Identify the blood parasite species.
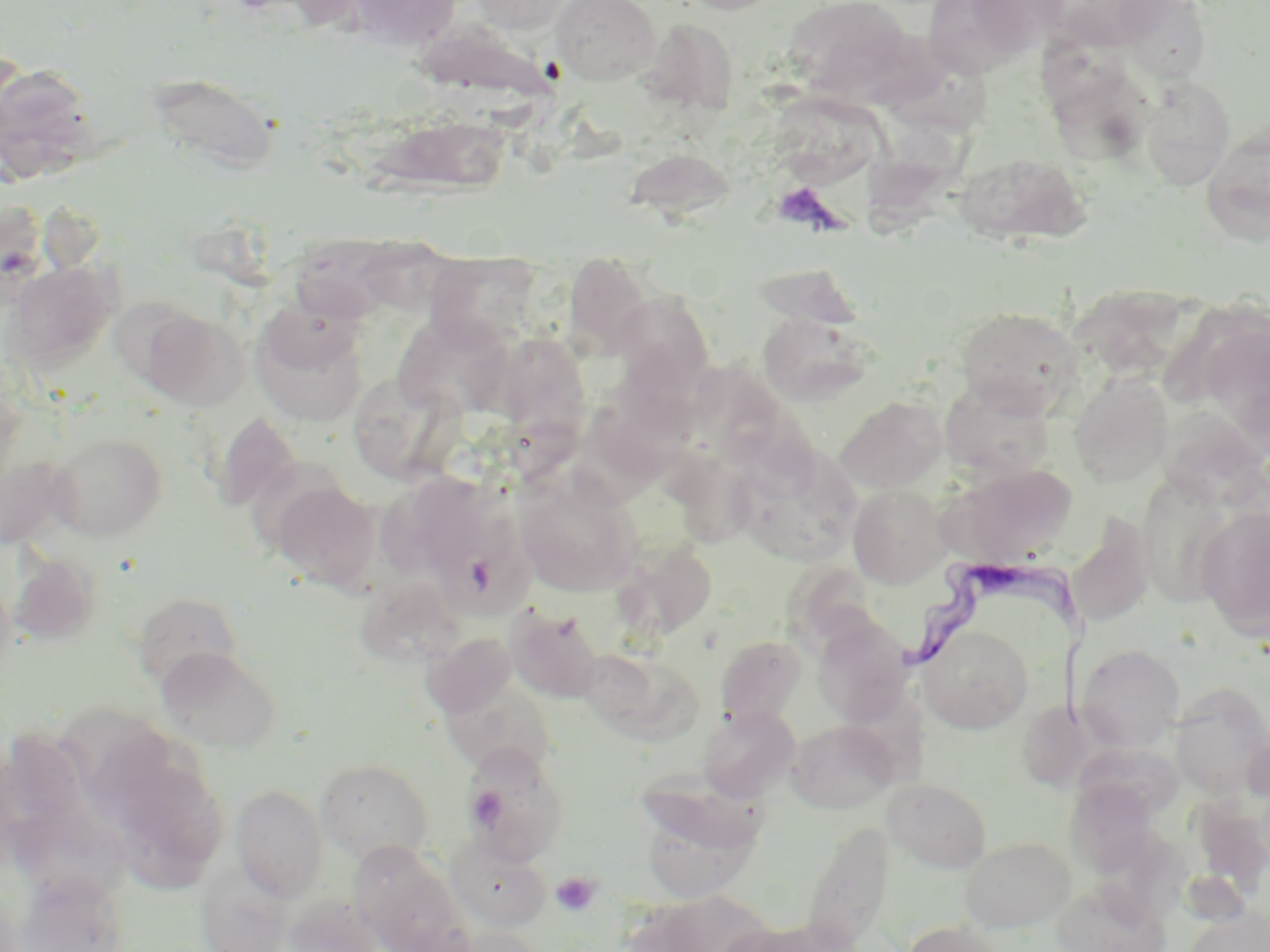

Trypanosoma brucei.

Summary:
  - Coordinate format: approximate bounding boxes as (x1,y1)-(x2,y2) corner pairs in pixels
  - Uninfected red blood cell locations: (344,0)-(461,51), (469,0)-(574,33), (552,0)-(661,85), (672,0)-(787,15), (785,0)-(911,99), (926,0)-(1064,71), (1044,0)-(1176,52), (1117,1)-(1212,83), (637,16)-(740,122), (884,37)-(993,137), (1,61)-(101,186), (1053,69)-(1163,166), (147,73)-(279,176), (1140,77)-(1235,189), (766,89)-(885,186), (374,113)-(510,199), (1201,119)-(1270,244), (865,126)-(984,238), (623,147)-(737,225), (952,151)-(1090,246), (289,234)-(406,322), (425,251)-(541,347), (564,252)-(654,358), (5,260)-(117,371), (753,264)-(865,330), (1069,283)-(1197,384), (614,291)-(714,391), (110,297)-(204,389), (954,307)-(1084,415), (141,309)-(249,410), (1199,312)-(1270,453), (251,313)-(368,427), (759,314)-(872,405), (395,319)-(517,418), (498,324)-(592,451), (698,368)-(816,487), (1069,373)-(1174,486), (351,376)-(475,485), (940,379)-(1056,481), (592,385)-(704,484), (836,396)-(946,494), (1157,404)-(1268,510), (212,413)-(301,514), (47,432)-(168,540), (661,444)-(769,556), (737,445)-(862,566), (943,463)-(1078,567), (514,469)-(641,597), (1135,473)-(1242,609), (386,476)-(495,577), (269,479)-(380,592), (848,484)-(950,588), (1196,505)-(1270,642), (435,514)-(540,617), (1068,514)-(1155,629), (618,542)-(717,640), (9,550)-(101,645), (363,582)-(469,665), (133,592)-(243,688), (506,606)-(605,703), (812,614)-(913,725), (919,624)-(1033,733), (423,632)-(517,718), (715,635)-(807,726), (1077,644)-(1184,751), (156,646)-(282,754), (583,651)-(704,745), (441,676)-(558,778), (1170,683)-(1270,799), (1017,699)-(1099,792), (59,705)-(177,812), (697,705)-(799,801), (785,718)-(899,813), (461,744)-(567,865), (106,753)-(226,891), (316,759)-(434,864), (635,765)-(776,852), (883,777)-(992,873), (1064,778)-(1160,876), (231,784)-(329,901), (638,797)-(762,901), (1191,798)-(1270,895), (11,803)-(128,904), (803,821)-(893,952), (447,834)-(550,930), (959,836)-(1075,932), (351,845)-(473,952), (196,870)-(293,952), (15,872)-(128,952), (1051,880)-(1171,952), (285,894)-(384,952), (1185,906)-(1269,952), (720,918)-(847,952), (902,920)-(1006,952), (436,924)-(544,952)
  - Platelet locations: (771,180)-(838,232), (468,786)-(506,827), (550,871)-(602,916)
  - Trypanosoma brucei locations: (896,560)-(1110,726)
  - Stain: May-Grünwald-Giemsa
  - Modality: light microscopy
  - Field of view: one of a larger specimen
  - Image size: 1270×952 pixels
  - Preparation: thin blood film
  - Magnification: 1000x